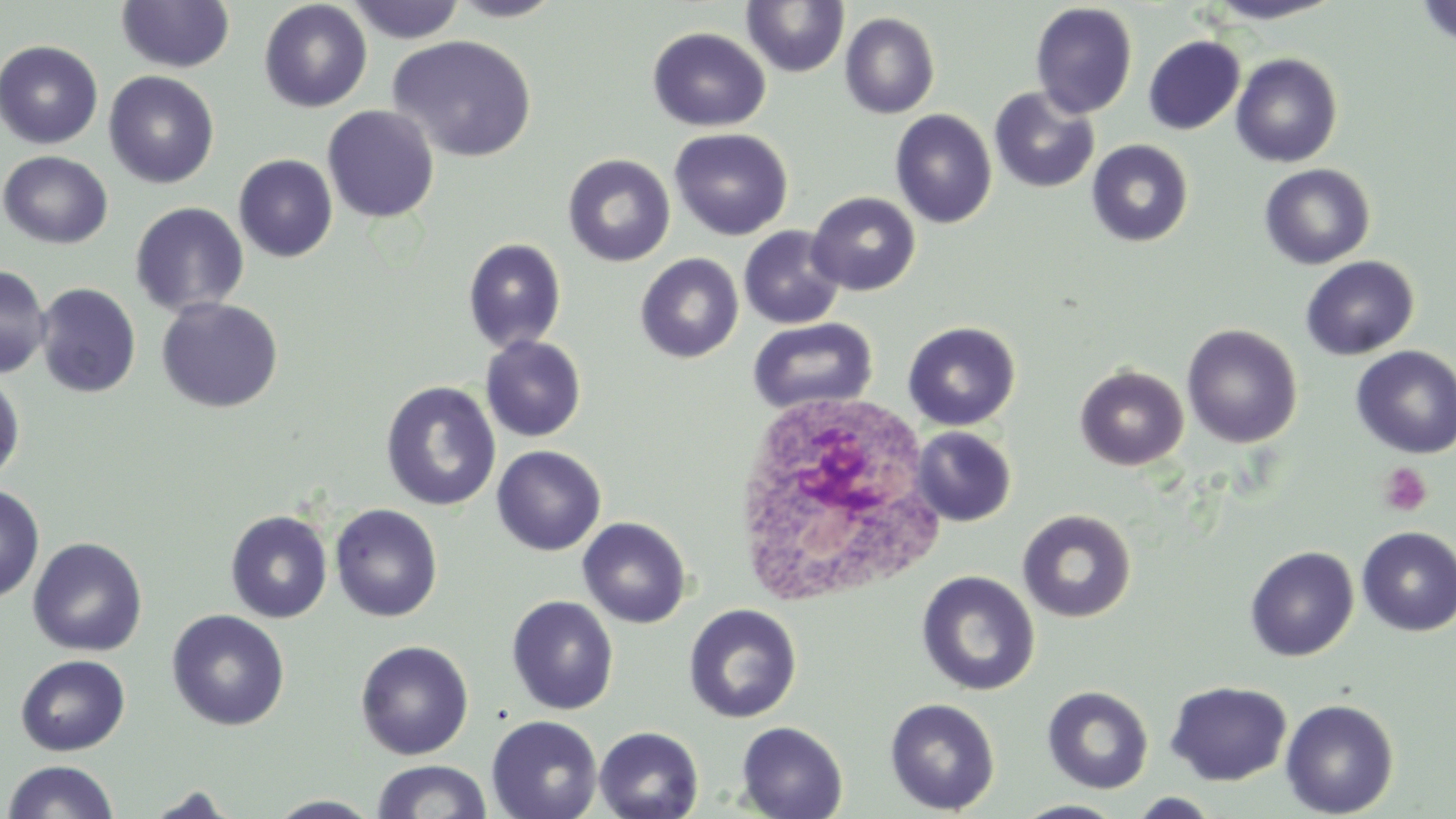
Summary:
  - Coordinate format: approximate bounding boxes as [x1, y1, x2, y2] in pixels
  - Platelet locations: [1377, 462, 1433, 518]
  - White blood cell locations: [728, 390, 950, 611]
  - Uninfected red blood cell locations: [115, 0, 235, 73], [447, 0, 567, 22], [1203, 0, 1346, 24], [1416, 0, 1456, 47], [259, 1, 372, 113], [345, 1, 467, 44], [742, 1, 850, 77], [1030, 2, 1138, 118], [840, 12, 940, 119], [647, 27, 771, 132], [389, 35, 538, 162], [1143, 36, 1244, 135], [0, 40, 103, 149], [1231, 53, 1343, 168], [104, 70, 219, 188], [989, 87, 1100, 193], [322, 105, 439, 223], [890, 108, 998, 228], [670, 128, 793, 240], [1087, 140, 1193, 247], [1, 150, 114, 249], [233, 154, 338, 262], [562, 154, 676, 266], [1259, 164, 1376, 269], [807, 191, 921, 295], [129, 202, 249, 317], [739, 226, 846, 329], [463, 238, 566, 352], [636, 253, 743, 363], [1300, 255, 1419, 360], [0, 264, 52, 379], [35, 283, 141, 398], [155, 297, 283, 413], [747, 317, 878, 416], [902, 321, 1021, 431], [1182, 324, 1302, 447], [480, 335, 587, 442], [1351, 345, 1456, 459], [1075, 365, 1189, 470], [0, 371, 25, 485], [381, 380, 502, 511], [911, 426, 1017, 527], [492, 445, 606, 555], [0, 483, 44, 603], [330, 503, 443, 622], [1017, 509, 1137, 623], [225, 510, 332, 623], [578, 516, 691, 628], [1356, 526, 1456, 636], [27, 536, 148, 656], [1245, 546, 1359, 661], [917, 571, 1039, 696], [506, 595, 619, 715], [684, 604, 802, 723], [167, 609, 290, 731], [354, 640, 474, 761], [15, 654, 130, 756], [1165, 680, 1292, 785], [1042, 685, 1154, 794], [884, 697, 1000, 815], [1280, 698, 1400, 817], [486, 715, 603, 819], [736, 721, 848, 819], [594, 726, 704, 819], [1, 760, 121, 818], [370, 760, 493, 819], [141, 787, 241, 818], [1125, 792, 1223, 818], [266, 795, 382, 817], [1012, 800, 1128, 819]
  - Slide-level diagnosis: negative for blood parasites
  - Magnification: 1000x
  - Field of view: one of a larger specimen
  - Stain: May-Grünwald-Giemsa
  - Modality: optical microscopy
  - Image size: 1456×819 pixels
  - Preparation: thin blood smear